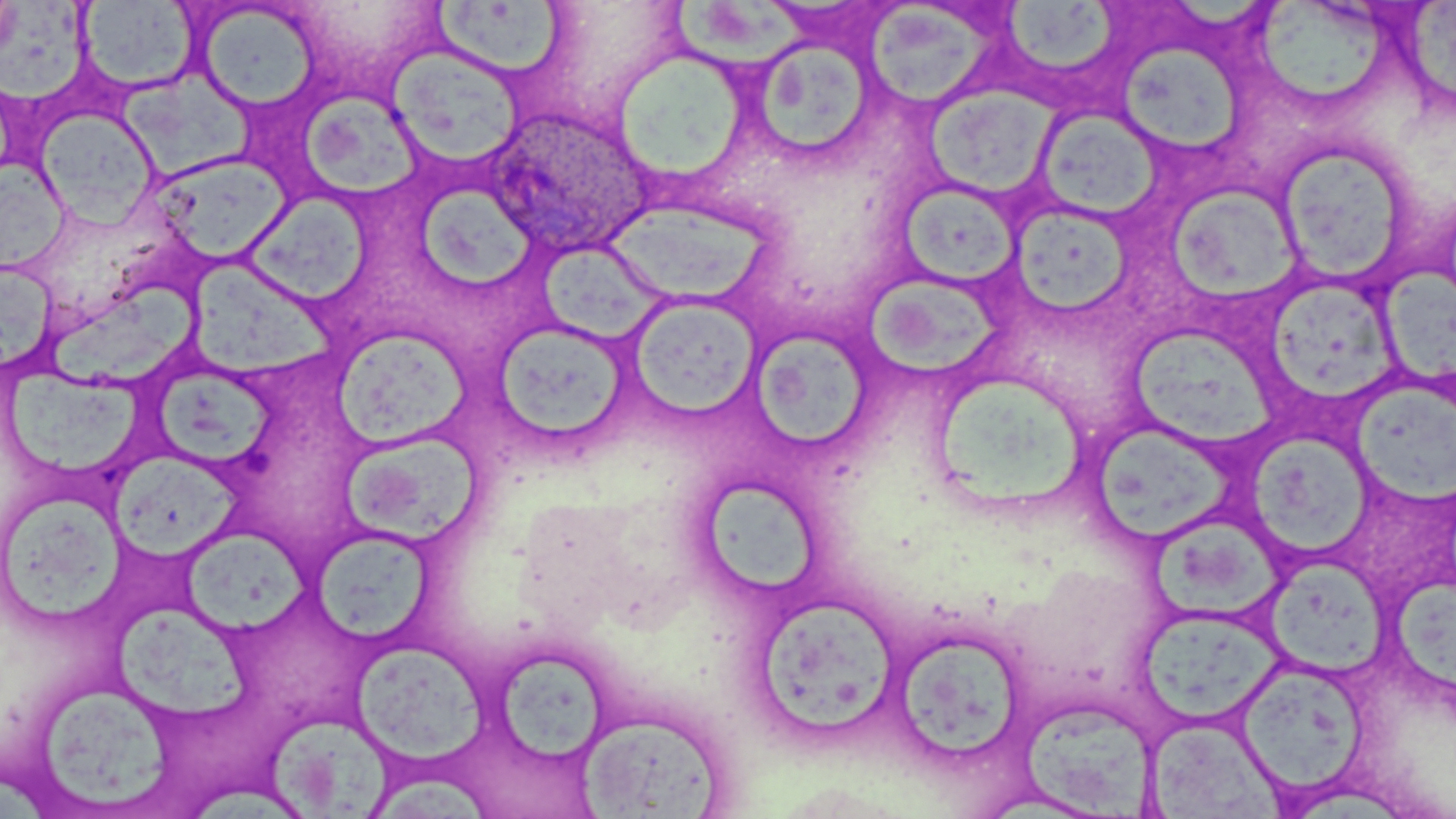
Summary:
  - Coordinate format: approximate bounding boxes as (x1,y1)-(x2,y2) corner pairs in pixels
  - Plasmodium ovale-infected red blood cell locations: (482,107)-(655,259)
  - Platelet locations: (241,448)-(277,483)
  - Uninfected red blood cell locations: (4,0)-(99,108), (664,0)-(816,72), (1405,0)-(1456,105), (79,1)-(199,93), (434,2)-(568,78), (1003,2)-(1125,74), (195,3)-(322,112), (1262,3)-(1393,98), (863,7)-(1001,111), (763,42)-(873,157), (1119,43)-(1242,153), (388,46)-(525,170), (611,49)-(754,188), (111,70)-(260,180), (926,88)-(1055,197), (297,93)-(422,202), (1034,108)-(1163,221), (37,109)-(159,227), (1274,142)-(1414,288), (148,153)-(293,263), (0,160)-(70,273), (412,182)-(527,285), (901,182)-(1020,289), (1167,187)-(1299,304), (245,191)-(371,305), (1006,199)-(1136,321), (599,203)-(776,306), (535,242)-(674,342), (0,259)-(59,374), (185,262)-(342,376), (1380,270)-(1456,381), (867,275)-(1008,375), (48,277)-(200,392), (1263,281)-(1406,400), (626,294)-(762,421), (487,321)-(633,450), (751,324)-(873,451), (331,328)-(470,449), (1130,328)-(1284,443), (3,365)-(142,473), (153,369)-(277,473), (1350,377)-(1456,511), (940,381)-(1094,515), (1097,431)-(1235,542), (1249,434)-(1377,560), (340,435)-(492,545), (105,451)-(248,558), (705,479)-(823,591), (2,484)-(127,624), (1154,522)-(1286,625), (310,525)-(436,644), (188,527)-(314,632), (1270,565)-(1388,682), (1390,577)-(1456,692), (752,594)-(901,740), (115,606)-(256,717), (1137,608)-(1284,717), (900,637)-(1020,758), (351,638)-(488,765), (499,653)-(610,763), (1227,668)-(1360,804), (43,692)-(178,809), (1023,706)-(1154,819), (578,712)-(728,817), (1147,715)-(1286,818), (271,717)-(389,818), (373,774)-(497,817), (193,781)-(298,819)
  - Slide-level diagnosis: Plasmodium ovale
  - Modality: light microscopy
  - Stain: May-Grünwald-Giemsa
  - Preparation: thin blood film
  - Field of view: one of a larger specimen
  - Image size: 1456×819 pixels
  - Magnification: 1000x